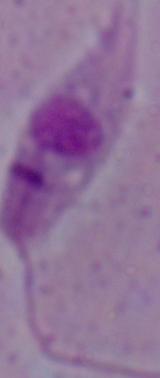
{
  "magnification": "1000x",
  "identification": "Leishmania",
  "modality": "micrograph"
}